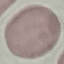
Summary:
  - Malaria status: uninfected
  - Image type: automatically extracted cell patch, resized to 64 × 64 pixels
  - Preparation: thin blood smear
  - Stain: Giemsa
  - Capture: smartphone camera at the microscope eyepiece